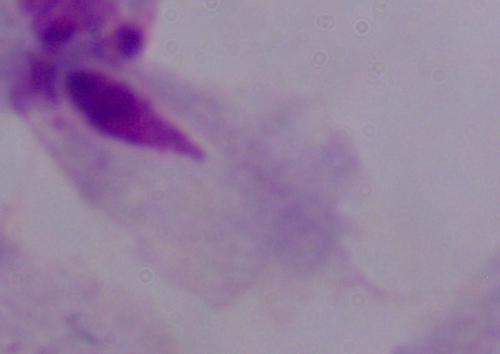 Photomicrograph. Captured at 1000x magnification. A trichomonad is shown.